Classify this cell by malaria status.
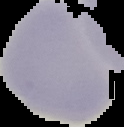
Uninfected.

Summary:
  - Image type: cell region segmented out of the field of view; surrounding area masked to black
  - Preparation: thin blood film
  - Image size: 124×127 pixels